Report the malaria status of this cell.
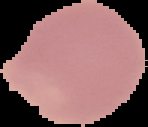
It is uninfected.

Summary:
  - Preparation: thin blood smear
  - Image size: 148×127 pixels
  - Image type: segmented cell region with the area outside set to black